Outline platelets.
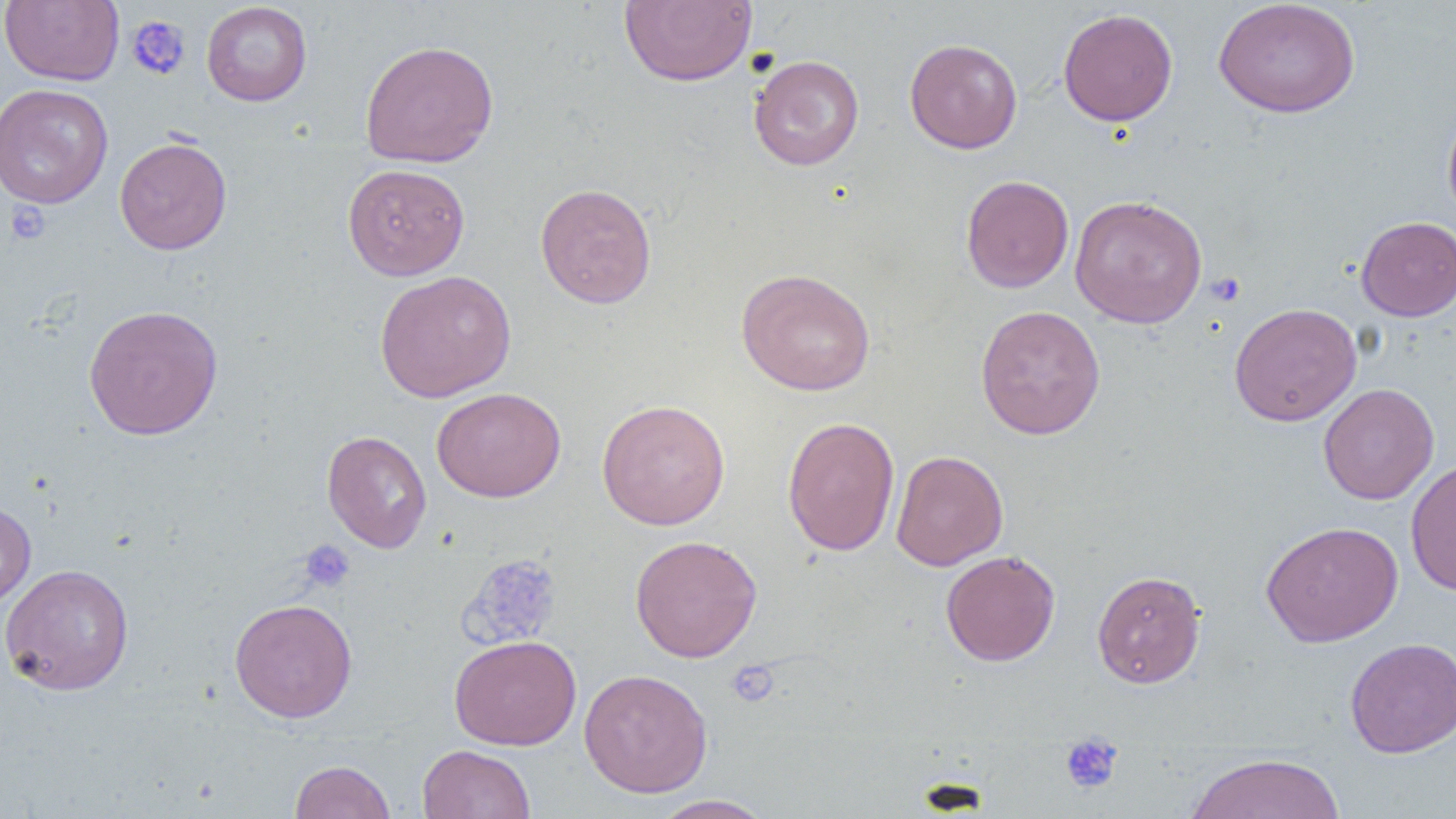
Approximate bounding boxes as [x1, y1, x2, y2] in pixels.
Platelets: [126, 15, 190, 80], [5, 201, 51, 245], [1206, 272, 1246, 306], [298, 539, 356, 593], [457, 552, 563, 650], [726, 660, 780, 707], [1060, 732, 1124, 794].

{
  "slide_level_diagnosis": "no evidence of blood parasites",
  "modality": "optical microscopy",
  "field_of_view": "single",
  "image_size": "1456×819 pixels",
  "preparation": "thin blood film",
  "uninfected_red_blood_cell_locations": "approximate bounding boxes as [x1, y1, x2, y2] in pixels: [0, 0, 124, 86], [619, 0, 757, 87], [1213, 1, 1360, 118], [201, 2, 312, 106], [1058, 8, 1178, 127], [904, 38, 1022, 154], [360, 39, 499, 168], [749, 54, 865, 170], [0, 83, 113, 209], [1442, 106, 1456, 225], [114, 136, 232, 255], [342, 163, 470, 281], [960, 175, 1074, 293], [534, 182, 657, 309], [1069, 194, 1208, 328], [1356, 216, 1456, 321], [735, 268, 876, 396], [374, 270, 517, 402], [1228, 302, 1362, 426], [83, 304, 223, 440], [975, 305, 1106, 440], [1318, 384, 1439, 505], [432, 387, 566, 502], [596, 399, 730, 530], [782, 416, 900, 556], [321, 430, 431, 553], [891, 449, 1008, 571], [1405, 457, 1456, 596], [0, 501, 37, 611], [1261, 521, 1403, 647], [629, 534, 763, 663], [940, 550, 1060, 666], [0, 563, 135, 696], [1092, 570, 1206, 688], [229, 598, 358, 723], [449, 634, 581, 751], [1345, 637, 1456, 758], [579, 668, 713, 797], [417, 744, 536, 819], [1184, 753, 1347, 818], [289, 759, 396, 819], [650, 794, 776, 819]",
  "magnification": "1000x"
}